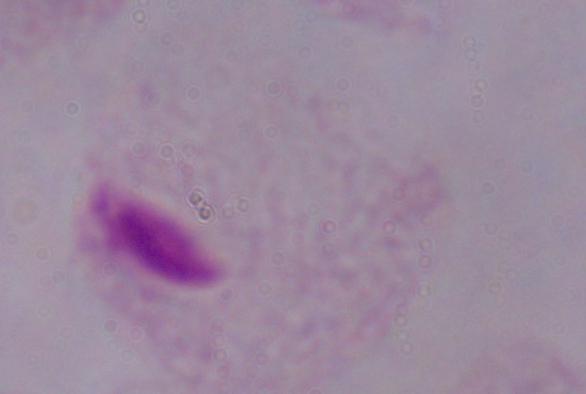
Summary:
  - Identification: trichomonad
  - Modality: photomicrograph
  - Magnification: 1000x